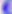

Summary:
  - Modality: photomicrograph
  - Identification: Toxoplasma gondii
  - Magnification: 400x